Assess the morphology of the erythrocytes.
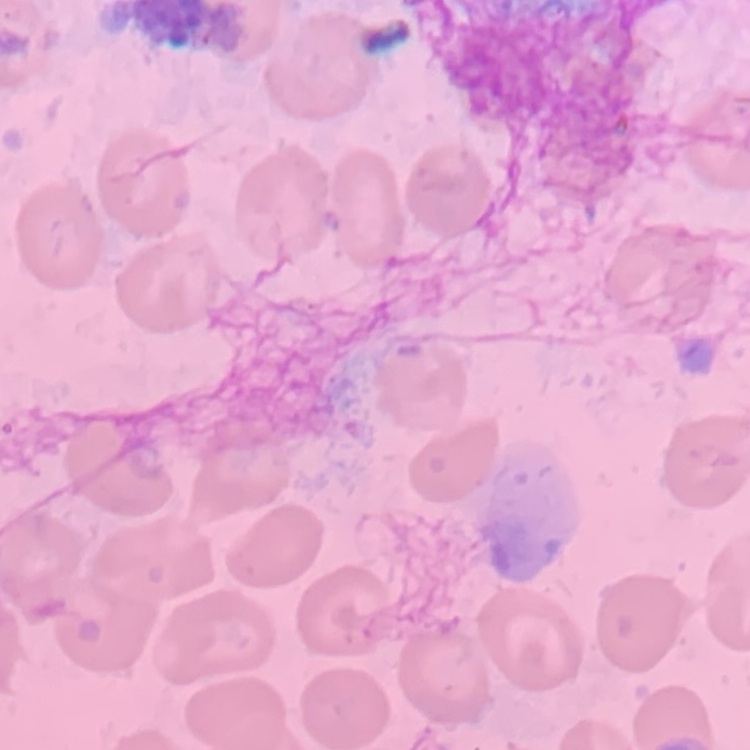

No rouleaux formation.

Thin blood film. One tile cut from a larger photomicrograph. Field's or Giemsa stain.